Locate every uninfected red blood cell.
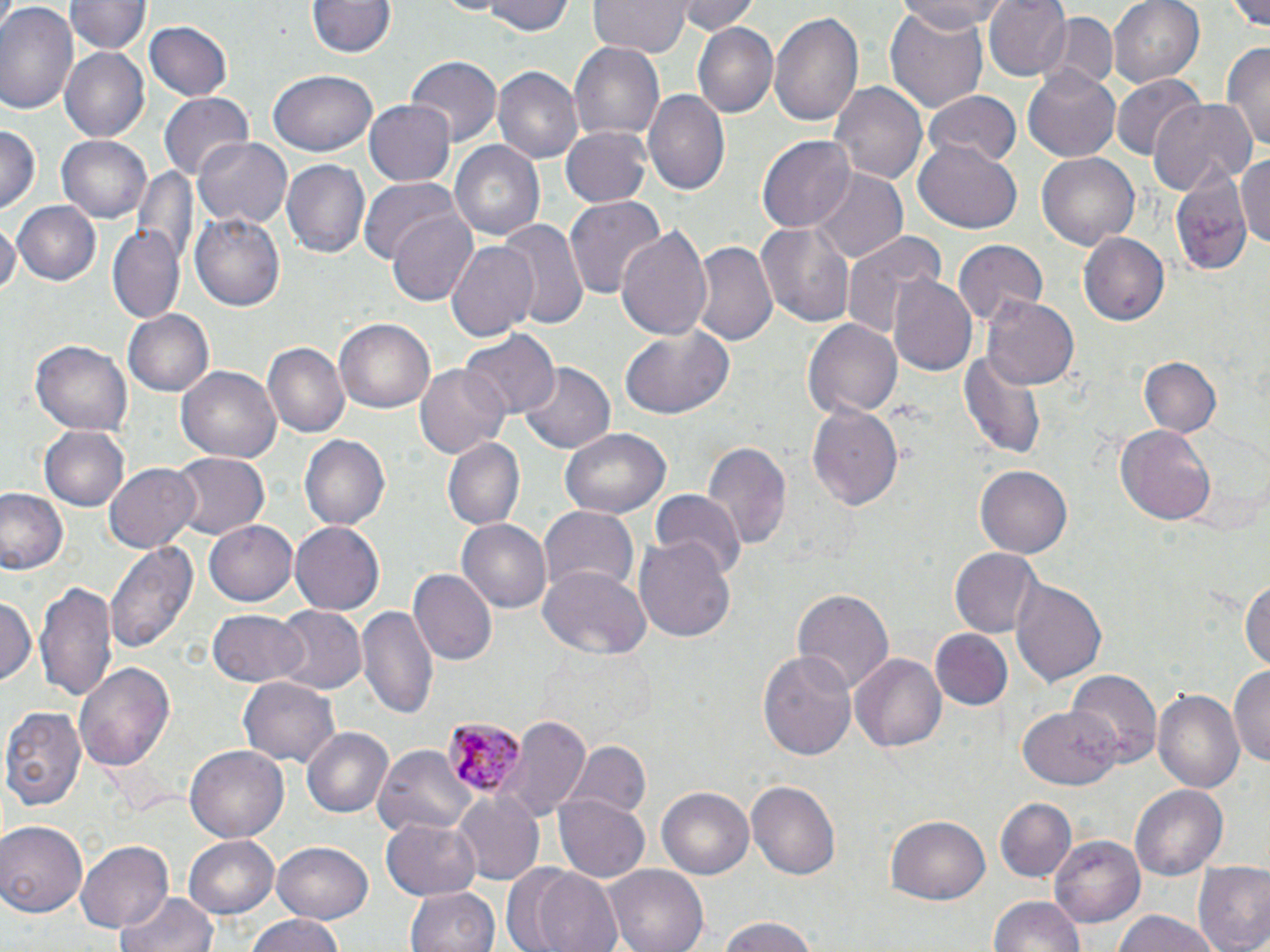

Approximate bounding boxes as (x1,y1)-(x2,y2) corner pairs in pixels.
Uninfected red blood cells: (69,0)-(149,57), (476,0)-(575,36), (679,0)-(760,36), (895,0)-(1009,34), (983,0)-(1069,80), (1108,0)-(1204,88), (1227,0)-(1270,33), (588,1)-(689,56), (0,2)-(80,118), (306,2)-(394,58), (769,7)-(864,131), (885,7)-(991,113), (1032,11)-(1122,96), (146,21)-(233,102), (692,22)-(779,119), (568,41)-(667,141), (1223,42)-(1270,155), (59,46)-(150,143), (407,58)-(500,145), (492,65)-(583,164), (1023,70)-(1119,162), (267,71)-(379,156), (1112,76)-(1205,162), (832,80)-(927,188), (646,88)-(731,196), (924,88)-(1022,169), (161,93)-(255,181), (1147,98)-(1256,198), (364,101)-(454,184), (0,125)-(40,214), (560,126)-(654,209), (57,134)-(152,223), (194,136)-(293,230), (757,136)-(856,232), (450,139)-(547,239), (915,142)-(1023,235), (1236,153)-(1270,248), (1035,154)-(1140,252), (279,158)-(370,259), (1166,163)-(1256,280), (133,165)-(196,265), (812,168)-(906,266), (359,177)-(458,264), (566,197)-(663,303), (11,199)-(101,285), (388,209)-(480,307), (192,211)-(288,312), (500,217)-(589,330), (0,218)-(18,304), (756,219)-(856,329), (107,223)-(183,321), (615,226)-(713,344), (841,228)-(944,336), (1079,232)-(1169,326), (693,238)-(779,350), (953,239)-(1049,328), (448,240)-(540,343), (888,277)-(977,375), (981,292)-(1079,391), (123,309)-(213,396), (802,317)-(902,420), (334,319)-(436,414), (619,324)-(734,421), (461,331)-(560,419), (32,339)-(133,438), (264,342)-(351,441), (959,348)-(1046,458), (1139,357)-(1222,438), (516,361)-(614,456), (176,363)-(282,461), (415,363)-(511,458), (807,403)-(905,511), (1115,422)-(1216,523), (40,424)-(130,511), (559,427)-(668,520), (298,434)-(391,533), (441,437)-(525,532), (703,440)-(789,551), (168,452)-(270,540), (104,461)-(200,554), (975,463)-(1073,558), (0,488)-(68,575), (650,490)-(744,579), (538,507)-(638,593), (455,518)-(551,615), (203,519)-(299,605), (289,521)-(386,613), (635,537)-(736,641), (105,538)-(200,653), (949,547)-(1044,639), (537,566)-(650,659), (408,568)-(497,667), (1240,574)-(1269,676), (1010,578)-(1107,689), (36,581)-(117,706), (790,587)-(893,696), (0,597)-(36,690), (273,605)-(368,694), (356,605)-(436,719), (207,610)-(309,687), (929,629)-(1013,709), (758,648)-(858,762), (850,652)-(947,754), (73,661)-(176,773), (1230,663)-(1270,767), (1066,669)-(1163,767), (239,675)-(340,768), (1153,688)-(1245,797), (1022,702)-(1123,787), (2,705)-(88,813), (507,717)-(592,818), (302,726)-(395,819), (568,742)-(650,824), (374,744)-(474,836), (186,746)-(289,842), (746,778)-(842,880), (1131,784)-(1228,881), (657,787)-(754,881), (452,791)-(546,887), (555,795)-(647,882), (994,796)-(1077,881), (885,816)-(990,903), (381,817)-(482,899), (0,821)-(88,915), (183,834)-(280,918), (1052,834)-(1145,923), (273,840)-(374,923), (75,841)-(174,934), (1193,861)-(1270,952), (518,864)-(625,952), (607,864)-(707,952), (404,885)-(499,952), (114,891)-(218,952), (988,896)-(1087,952), (1109,910)-(1224,952), (241,912)-(349,952), (713,915)-(825,952).

Plasmodium malariae-infected red blood cell locations: (441,714)-(523,801). Slide-level diagnosis: Plasmodium malariae. Thin blood smear. May-Grünwald-Giemsa-stained preparation. Image is 1270×952 pixels. Captured at 1000x magnification. Single field of view. Light microscopy.